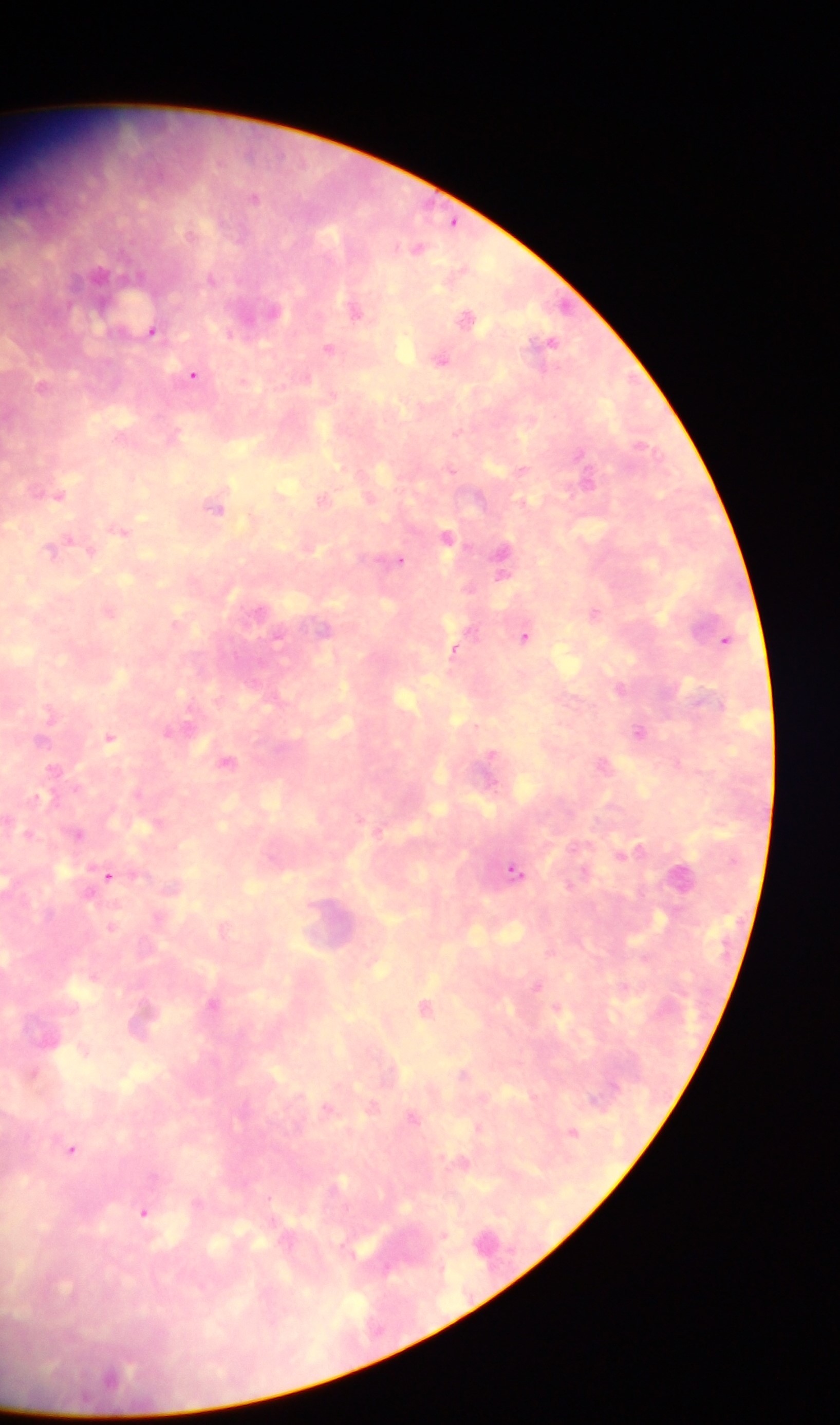

Approximate centers as x y in pixels.
Summary:
  - Plasmodium parasite locations: 253 197; 452 223; 416 248; 98 274; 356 309; 269 311; 467 318; 152 330; 549 342; 328 349; 440 359; 193 374; 43 385; 520 469; 587 477; 58 492; 323 498; 215 505; 120 529; 446 536; 58 547; 503 555; 399 559; 109 610; 594 611; 324 628; 525 635; 725 639; 454 649; 620 689; 170 732; 640 732; 110 736; 228 761; 603 763; 54 770; 157 824; 25 833; 76 833; 621 854; 515 870; 109 875; 681 875; 223 928; 536 984; 213 1004; 425 1007; 144 1017; 85 1048; 33 1073; 463 1074; 533 1097; 372 1106; 327 1108; 413 1118; 477 1127; 571 1131; 71 1148; 461 1164; 143 1212
  - Preparation: thick blood smear
  - Capture: mobile-phone photograph through a microscope
  - Image size: 840×1425 pixels
  - Field of view: single
  - Country: Ghana